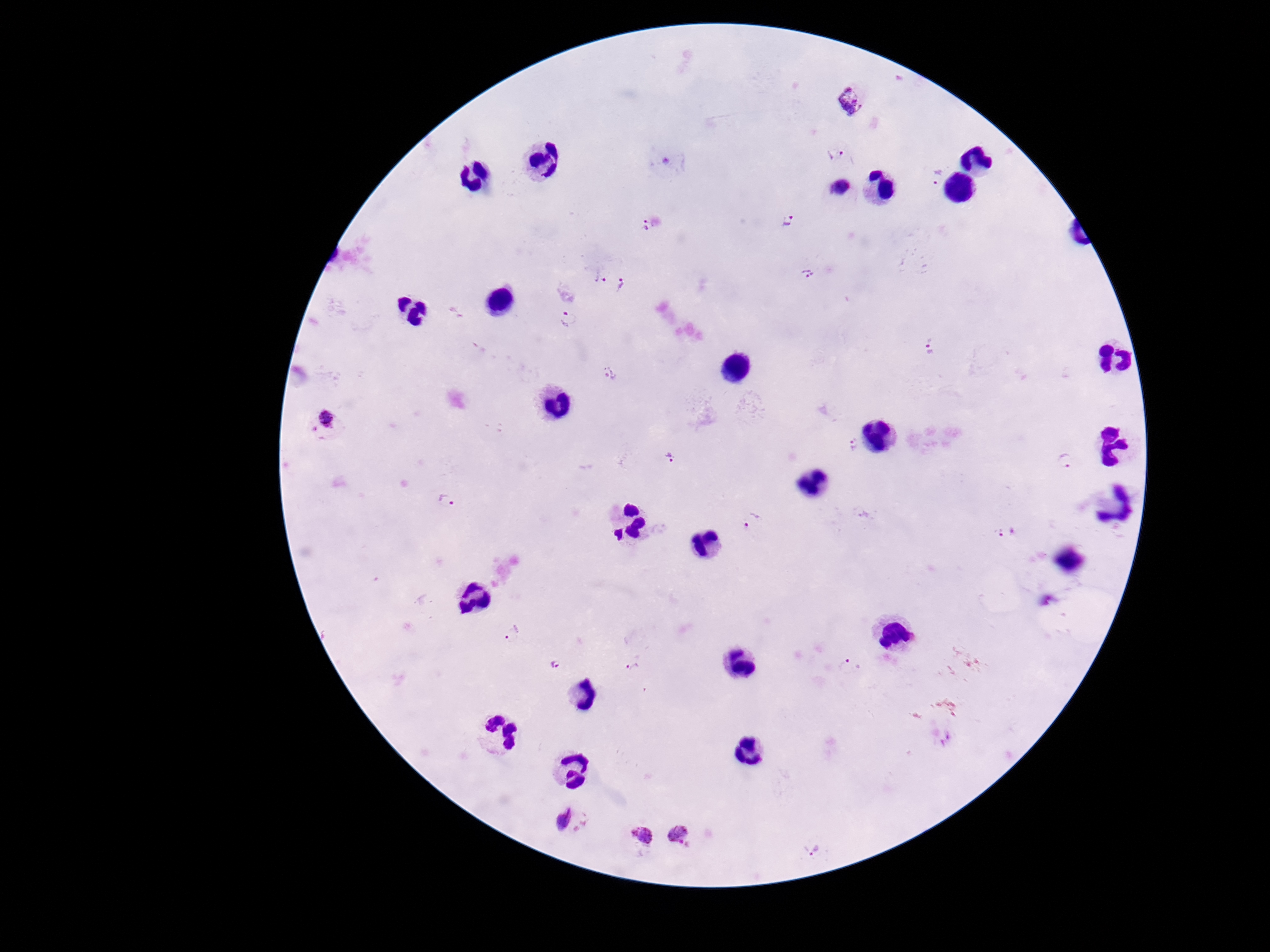
Approximate centers as [x, y] in pixels.
Summary:
  - Plasmodium parasite locations: [853, 101], [833, 153], [937, 177], [841, 188], [788, 220], [648, 224], [809, 273], [601, 278], [621, 285], [570, 318], [930, 353], [611, 374], [326, 422], [854, 445], [1066, 458], [670, 459], [448, 500], [752, 523], [1005, 532], [513, 634], [557, 665], [851, 666], [634, 668], [572, 822], [686, 834], [638, 835], [813, 852]
  - Capture: smartphone camera through the microscope eyepiece
  - Patient malaria status: positive
  - Preparation: thick peripheral-blood smear
  - Stain: Giemsa
  - Magnification: 100x
  - Image size: 1270×952 pixels
  - Field of view: one from this slide